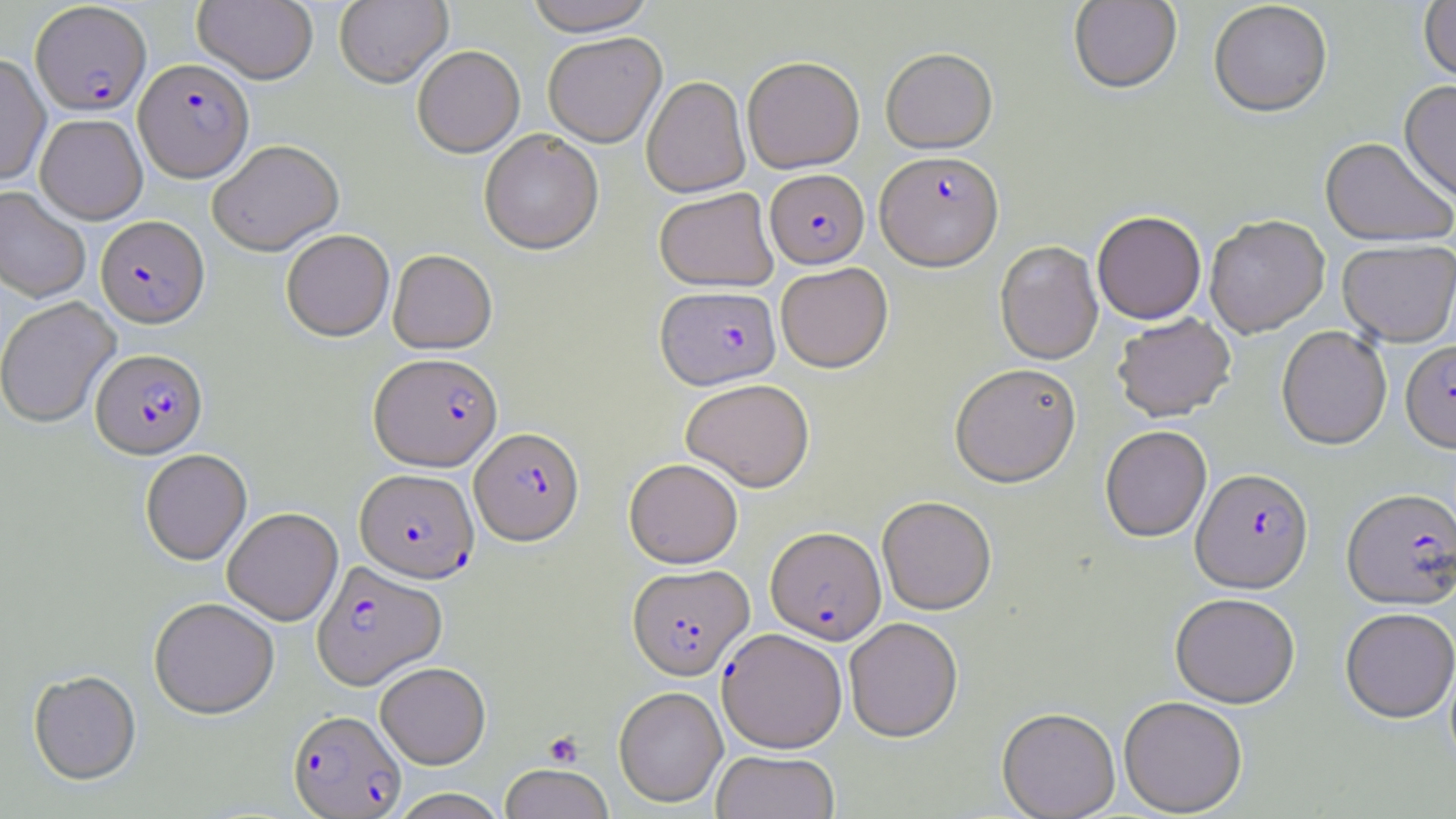

Approximate bounding boxes as named x1/y1/x2/y2 corners in pixels. Plasmodium falciparum-infected red blood cell locations: (x1=30, y1=3, x2=152, y2=117), (x1=133, y1=59, x2=254, y2=183), (x1=874, y1=152, x2=1004, y2=273), (x1=765, y1=170, x2=869, y2=269), (x1=96, y1=217, x2=209, y2=330), (x1=656, y1=286, x2=781, y2=391), (x1=1400, y1=341, x2=1456, y2=455), (x1=91, y1=349, x2=208, y2=460), (x1=368, y1=354, x2=502, y2=473), (x1=470, y1=428, x2=584, y2=547), (x1=354, y1=469, x2=479, y2=584), (x1=1191, y1=470, x2=1314, y2=596), (x1=1341, y1=491, x2=1456, y2=612), (x1=765, y1=527, x2=886, y2=644), (x1=312, y1=561, x2=447, y2=690), (x1=627, y1=564, x2=753, y2=680), (x1=717, y1=628, x2=847, y2=753), (x1=288, y1=709, x2=407, y2=818). Platelet locations: (x1=543, y1=730, x2=584, y2=768). Uninfected red blood cell locations: (x1=193, y1=0, x2=318, y2=86), (x1=334, y1=0, x2=453, y2=89), (x1=524, y1=0, x2=656, y2=38), (x1=1068, y1=0, x2=1182, y2=95), (x1=1418, y1=1, x2=1456, y2=87), (x1=1208, y1=3, x2=1333, y2=120), (x1=543, y1=34, x2=667, y2=149), (x1=412, y1=47, x2=525, y2=160), (x1=881, y1=48, x2=998, y2=156), (x1=0, y1=54, x2=50, y2=185), (x1=743, y1=57, x2=864, y2=174), (x1=642, y1=77, x2=750, y2=198), (x1=1398, y1=82, x2=1456, y2=208), (x1=35, y1=115, x2=147, y2=225), (x1=479, y1=131, x2=603, y2=257), (x1=1319, y1=139, x2=1455, y2=250), (x1=208, y1=143, x2=344, y2=258), (x1=0, y1=187, x2=90, y2=303), (x1=654, y1=188, x2=778, y2=292), (x1=1092, y1=213, x2=1206, y2=325), (x1=1205, y1=218, x2=1329, y2=340), (x1=281, y1=231, x2=394, y2=342), (x1=994, y1=241, x2=1104, y2=366), (x1=1338, y1=241, x2=1456, y2=348), (x1=387, y1=250, x2=497, y2=355), (x1=775, y1=263, x2=893, y2=374), (x1=0, y1=297, x2=121, y2=429), (x1=1112, y1=314, x2=1236, y2=424), (x1=1277, y1=327, x2=1392, y2=452), (x1=950, y1=364, x2=1082, y2=489), (x1=680, y1=379, x2=814, y2=492), (x1=1100, y1=427, x2=1212, y2=543), (x1=140, y1=450, x2=252, y2=565), (x1=624, y1=458, x2=743, y2=568), (x1=877, y1=496, x2=996, y2=615), (x1=223, y1=508, x2=343, y2=626), (x1=1170, y1=595, x2=1300, y2=709), (x1=149, y1=598, x2=279, y2=720), (x1=1340, y1=610, x2=1456, y2=725), (x1=844, y1=618, x2=963, y2=742), (x1=375, y1=662, x2=491, y2=769), (x1=28, y1=672, x2=142, y2=786), (x1=613, y1=686, x2=728, y2=807), (x1=1118, y1=697, x2=1248, y2=817), (x1=997, y1=708, x2=1120, y2=819), (x1=711, y1=750, x2=840, y2=819), (x1=499, y1=764, x2=614, y2=819), (x1=387, y1=788, x2=510, y2=819). Slide-level diagnosis: Plasmodium falciparum. One field of a larger specimen. 1000x magnification. Light microscopy. May-Grünwald-Giemsa-stained preparation. Image is 1456×819 pixels. Thin blood smear.